Give the position of every leukocyte visible.
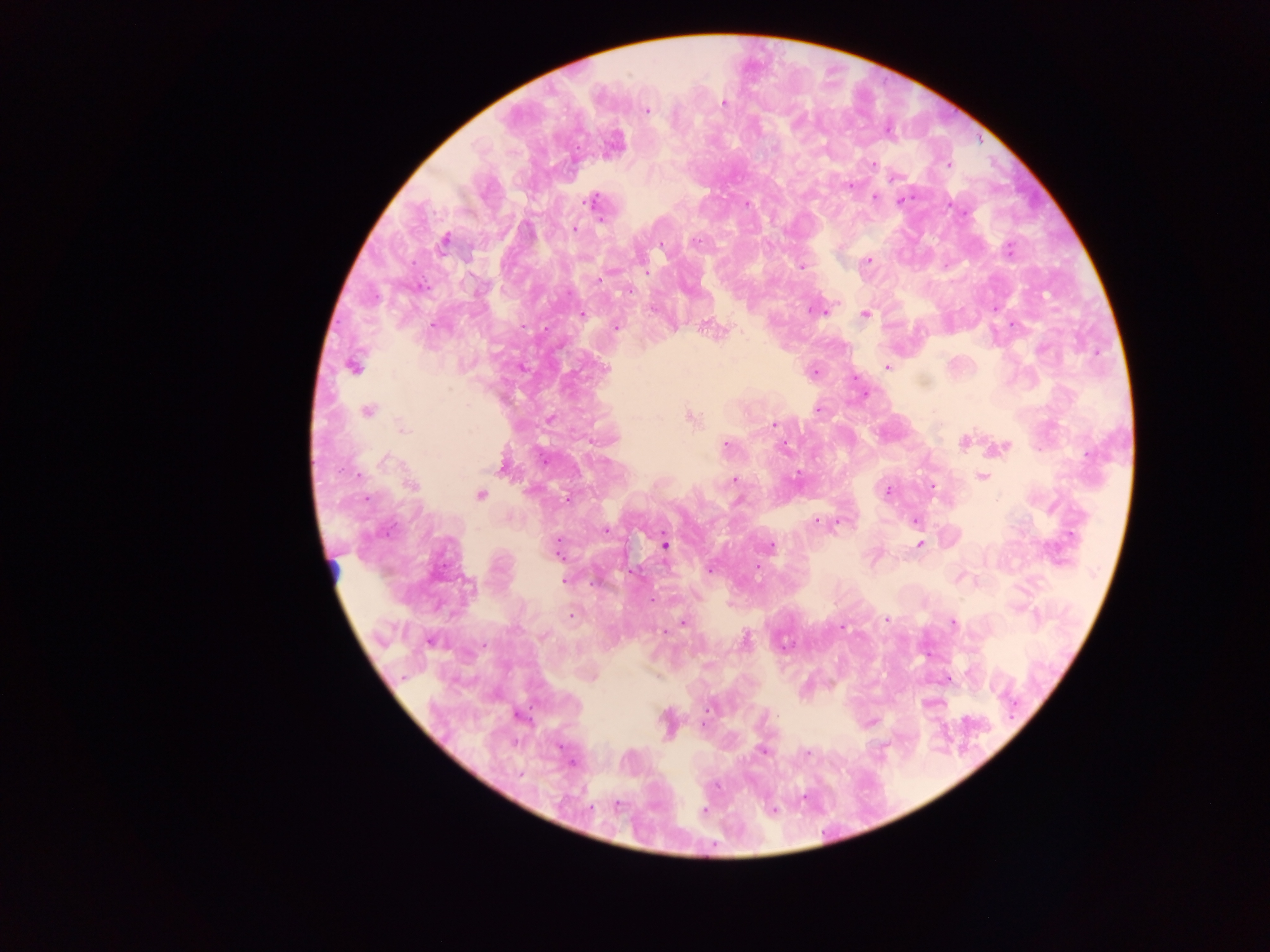
No leukocytes observed.

Approximate centers as (x, y) in pixels. Malaria parasite locations: (724, 103), (647, 110), (797, 122), (873, 164), (948, 164), (895, 176), (849, 185), (874, 198), (903, 199), (592, 202), (746, 205), (574, 229), (444, 241), (695, 241), (661, 245), (1009, 249), (868, 260), (802, 267), (630, 290), (812, 311), (865, 314), (583, 315), (706, 325), (434, 326), (616, 326), (886, 366), (353, 367), (814, 373), (818, 409), (368, 411), (690, 418), (550, 419), (773, 424), (403, 427), (964, 442), (727, 445), (1004, 446), (785, 447), (386, 461), (501, 467), (982, 477), (734, 481), (411, 485), (886, 491), (480, 495), (568, 499), (738, 501), (915, 521), (816, 522), (386, 531), (605, 531), (920, 544), (665, 546), (770, 547), (557, 548), (710, 571), (564, 580), (571, 617), (886, 619), (682, 623), (953, 623), (841, 627), (746, 640), (431, 642), (593, 678), (763, 751), (807, 753), (572, 764), (704, 810). Mobile-phone photograph taken through the microscope. Collected in Ghana. One field of view. Image is 1270×952 pixels. Thick blood film.